Classify this cell by malaria status.
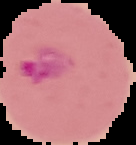

It is parasitized.

Summary:
  - Image type: segmented cell region on a black background
  - Preparation: thin blood film
  - Image size: 136×145 pixels